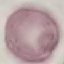

Summary:
  - Result: no malaria parasites detected
  - Capture: smartphone camera at the microscope eyepiece
  - Preparation: thin smear
  - Stain: Giemsa
  - Image type: automatically extracted cell patch, resized to 64 × 64 pixels